Locate every Plasmodium parasite.
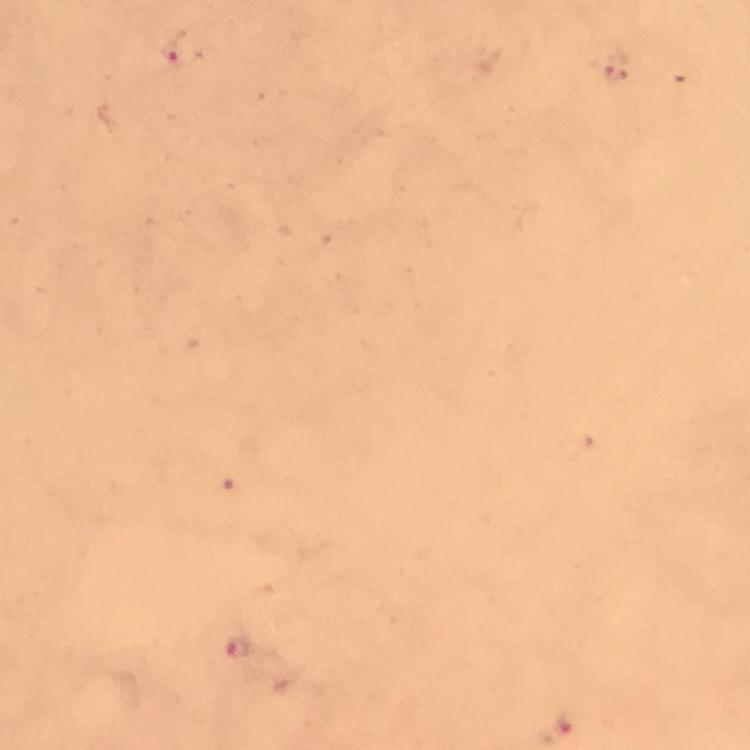
Approximate centers as [x, y] in pixels.
Plasmodium parasites: [183, 50], [613, 67], [239, 650], [566, 725].

Summary:
  - Immersion oil: used
  - Context: from a malaria diagnostic workup
  - Image size: 750×750 pixels
  - Preparation: thick blood film
  - Capture: smartphone mounted on the microscope
  - Cropped from: a single field of view
  - Magnification: 100x
  - Stain: Giemsa